Locate every blood parasite and identify its species.
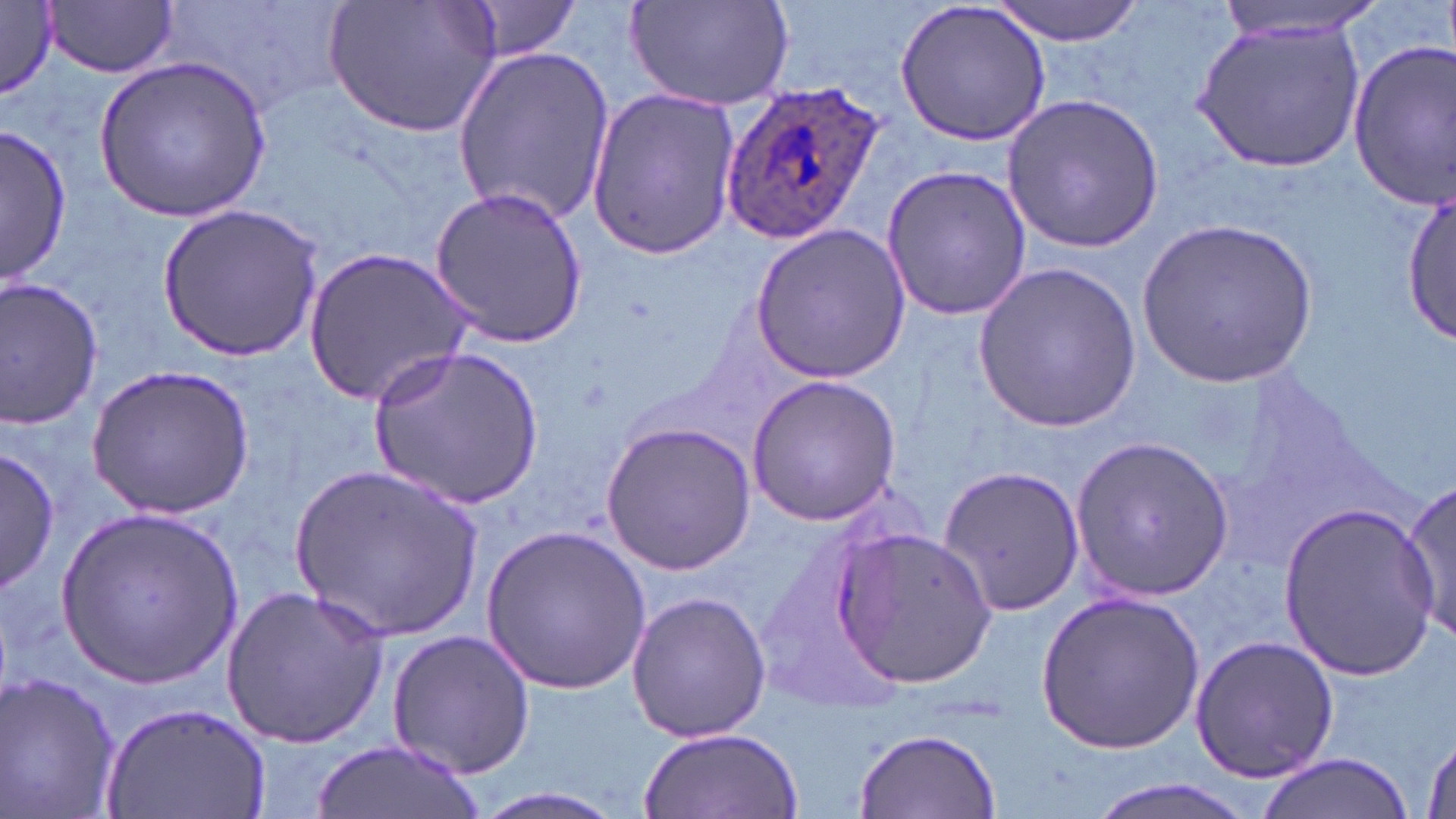
Approximate bounding boxes as (x1, y1, x2, y2) in pixels.
Plasmodium ovale-infected red blood cells: (718, 80, 885, 247).
No Plasmodium falciparum, Plasmodium malariae, Plasmodium vivax, Babesia divergens, or Trypanosoma brucei observed.

slide_level_diagnosis: Plasmodium ovale
uninfected_red_blood_cell_locations: 'approximate bounding boxes as (x1, y1, x2, y2) in pixels: (176, 0, 358, 114), (324, 0, 506, 140), (623, 0, 799, 113), (894, 0, 1054, 148), (991, 0, 1146, 44), (1219, 0, 1388, 41), (46, 1, 179, 78), (459, 1, 584, 61), (0, 3, 60, 100), (1192, 14, 1367, 171), (1347, 37, 1455, 207), (451, 48, 615, 225), (95, 54, 270, 224), (584, 86, 740, 260), (1000, 93, 1165, 254), (3, 123, 71, 285), (879, 161, 1033, 323), (425, 187, 587, 347), (1404, 189, 1453, 348), (158, 204, 324, 361), (1138, 219, 1318, 388), (750, 222, 911, 385), (302, 246, 476, 408), (974, 262, 1140, 434), (0, 277, 104, 430), (369, 347, 544, 509), (83, 362, 258, 521), (745, 375, 903, 526), (599, 421, 758, 574), (1069, 435, 1234, 602), (0, 447, 57, 597), (290, 462, 483, 643), (936, 463, 1085, 618), (1396, 478, 1456, 639), (1276, 500, 1438, 680), (59, 504, 243, 690), (482, 522, 653, 695), (832, 526, 998, 690), (220, 584, 390, 749), (626, 590, 772, 743), (1035, 591, 1208, 753), (385, 627, 539, 779), (1189, 633, 1339, 784), (0, 670, 125, 819), (107, 699, 270, 819), (639, 727, 806, 819), (854, 727, 1000, 819), (1418, 731, 1456, 819), (310, 738, 482, 819), (1255, 755, 1411, 819), (1082, 778, 1261, 819), (459, 787, 640, 819)'
image_size: 1456×819 pixels
magnification: 1000x
preparation: thin blood smear
field_of_view: single
modality: light microscopy
stain: May-Grünwald-Giemsa